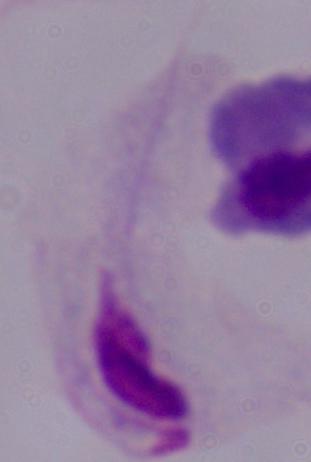
Summary:
  - Modality: micrograph
  - Magnification: 1000x
  - Identification: trichomonad